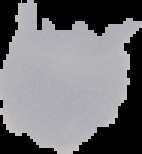

From a thin blood film. Result: no Plasmodium parasites seen. The area outside the segmented cell region is set to black. Image is 142×154 pixels.